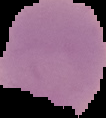

{
  "preparation": "thin blood film",
  "image_size": "106×118 pixels",
  "malaria_status": "uninfected",
  "image_type": "cell region segmented out of the field of view; surrounding area masked to black"
}